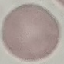
result = negative for malaria parasites
stain = Giemsa
capture = smartphone camera at the microscope eyepiece
preparation = thin blood smear
image type = cell patch, automatically extracted from a larger field of view and resized to 64 × 64 pixels